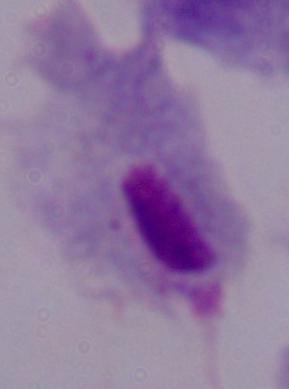
Summary:
  - Magnification: 1000x
  - Identification: trichomonad
  - Modality: micrograph